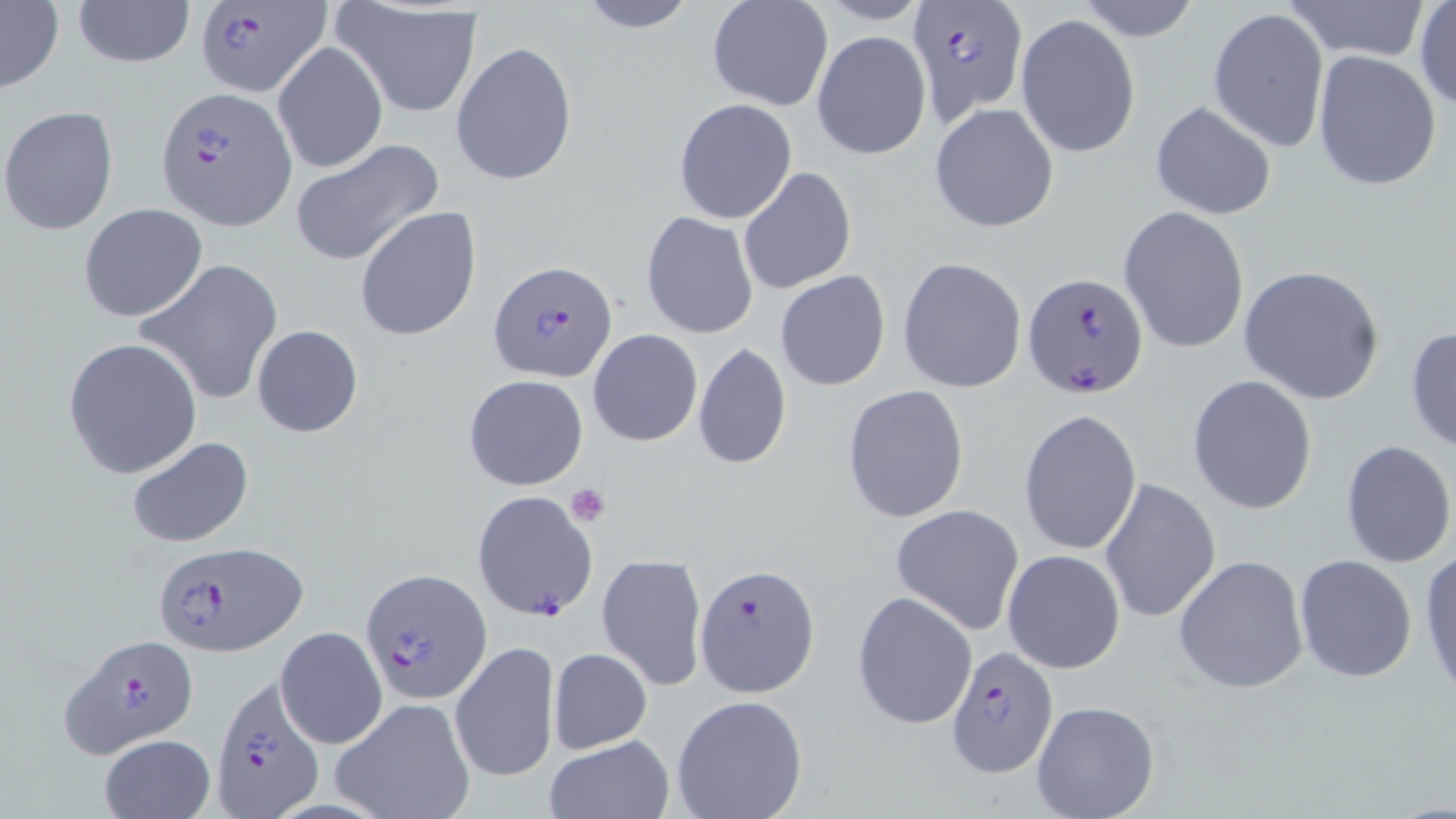

slide-level diagnosis = Plasmodium falciparum
magnification = 1000x
Plasmodium falciparum-infected red blood cell locations = approximate bounding boxes as (x1, y1, x2, y2) in pixels: (192, 0, 333, 98), (907, 0, 1029, 120), (157, 88, 296, 230), (489, 261, 618, 383), (1021, 271, 1149, 397), (471, 489, 600, 623), (151, 539, 305, 657), (694, 564, 821, 696), (363, 570, 491, 700), (62, 634, 196, 756), (946, 646, 1059, 777), (210, 677, 324, 816)
stain = May-Grünwald-Giemsa
image size = 1456×819 pixels
platelet locations = approximate bounding boxes as (x1, y1, x2, y2) in pixels: (564, 483, 613, 527)
preparation = thin blood film
modality = optical microscopy
uninfected red blood cell locations = approximate bounding boxes as (x1, y1, x2, y2) in pixels: (71, 0, 195, 70), (574, 0, 698, 32), (1072, 0, 1203, 43), (1286, 0, 1428, 63), (333, 1, 483, 116), (706, 1, 832, 112), (1414, 2, 1456, 112), (0, 3, 64, 92), (1208, 7, 1328, 151), (1016, 13, 1141, 158), (813, 30, 931, 159), (273, 40, 387, 175), (450, 40, 578, 186), (1312, 49, 1442, 191), (673, 98, 797, 224), (1149, 100, 1277, 219), (929, 102, 1059, 233), (1, 106, 117, 234), (290, 137, 445, 267), (737, 167, 857, 294), (77, 202, 207, 323), (356, 206, 483, 342), (1119, 206, 1249, 355), (641, 211, 759, 339), (897, 256, 1026, 394), (136, 259, 286, 405), (1237, 264, 1386, 405), (775, 269, 890, 392), (250, 324, 364, 437), (1405, 324, 1456, 454), (589, 330, 703, 446), (63, 337, 203, 479), (692, 341, 791, 469), (464, 374, 588, 490), (1187, 375, 1317, 514), (841, 385, 969, 525), (1018, 408, 1143, 556), (125, 435, 254, 549), (1339, 440, 1456, 569), (1099, 477, 1219, 625), (889, 504, 1024, 634), (1417, 544, 1456, 698), (1003, 549, 1125, 673), (596, 551, 708, 692), (1173, 553, 1309, 694), (1293, 554, 1418, 682), (853, 591, 976, 729), (276, 626, 386, 749), (451, 640, 560, 782), (549, 647, 651, 753), (670, 693, 808, 819), (331, 697, 474, 818), (1030, 698, 1161, 819), (98, 734, 216, 819), (542, 736, 674, 819)
field of view = single